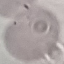

Summary:
  - Result: negative for malaria parasites
  - Preparation: thin blood smear
  - Capture: smartphone camera at the microscope eyepiece
  - Image type: automatically extracted cell patch, resized to 64 × 64 pixels
  - Stain: Giemsa